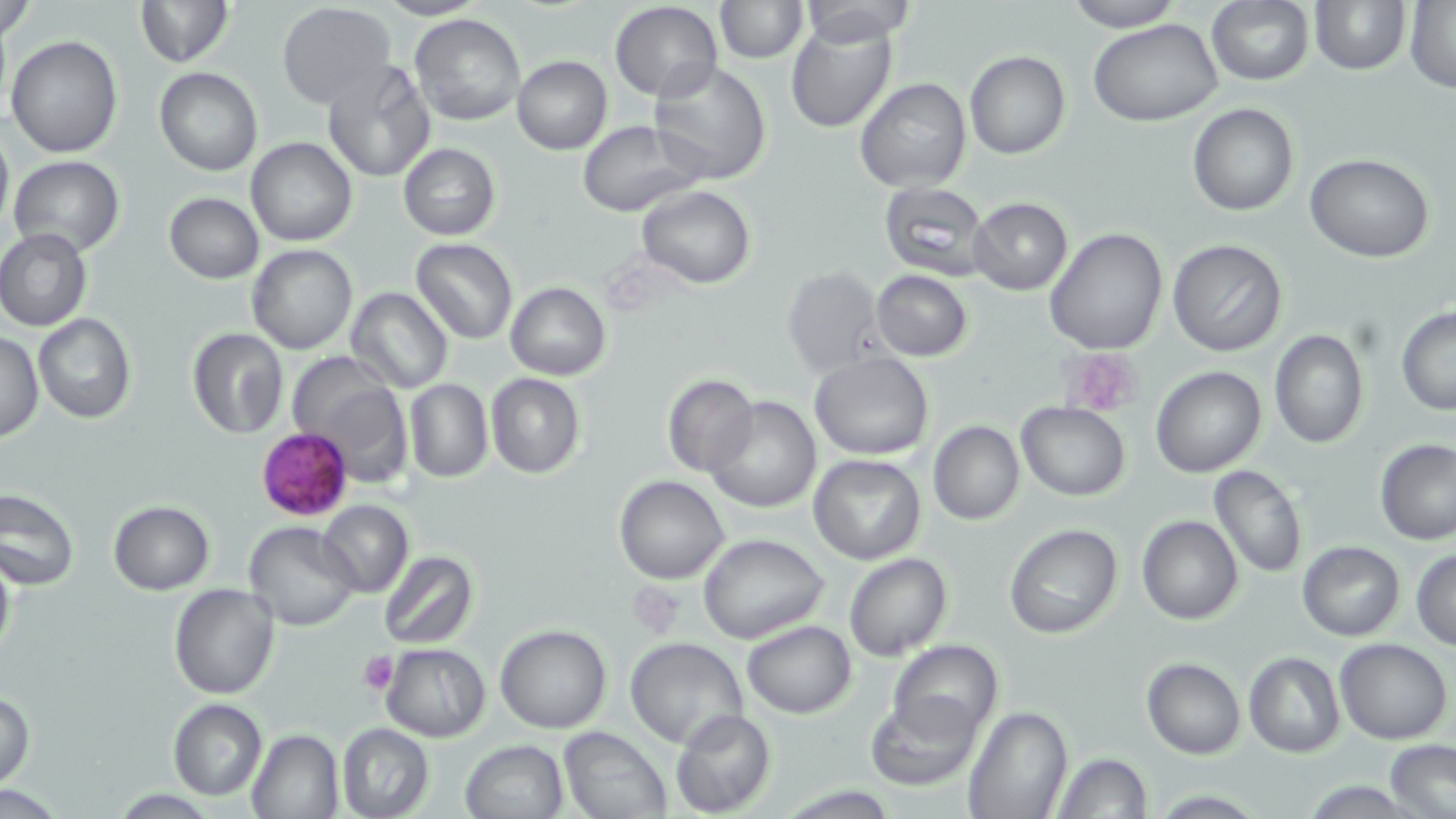

Summary:
  - Coordinate format: approximate bounding boxes as (x1, y1, x2, y2) in pixels
  - Plasmodium falciparum-infected red blood cell locations: (257, 427, 353, 518)
  - Uninfected red blood cell locations: (134, 0, 234, 67), (715, 0, 808, 63), (1309, 0, 1410, 74), (1, 1, 37, 44), (610, 1, 722, 100), (792, 1, 924, 45), (1064, 1, 1185, 31), (276, 2, 394, 110), (1206, 2, 1314, 85), (1403, 2, 1455, 92), (411, 14, 525, 126), (786, 16, 897, 133), (1089, 19, 1222, 126), (6, 33, 124, 157), (965, 50, 1071, 159), (512, 55, 612, 154), (645, 60, 770, 185), (321, 61, 435, 183), (155, 68, 263, 177), (854, 77, 971, 193), (1188, 103, 1298, 216), (576, 121, 701, 217), (0, 124, 13, 233), (245, 137, 357, 248), (398, 143, 500, 239), (1304, 153, 1435, 262), (8, 155, 127, 256), (878, 181, 992, 279), (637, 185, 756, 289), (164, 193, 264, 284), (970, 197, 1072, 293), (0, 227, 92, 332), (1044, 227, 1168, 355), (411, 238, 518, 345), (1168, 239, 1288, 356), (248, 244, 357, 354), (781, 265, 885, 379), (871, 270, 973, 361), (504, 282, 611, 380), (345, 286, 451, 393), (1395, 306, 1456, 414), (33, 314, 136, 423), (186, 328, 289, 440), (1268, 328, 1368, 448), (1, 329, 44, 442), (809, 351, 934, 459), (289, 358, 413, 486), (1151, 365, 1266, 478), (485, 372, 585, 479), (662, 373, 758, 476), (405, 379, 493, 483), (705, 395, 820, 512), (1015, 402, 1133, 500), (928, 422, 1025, 524), (1375, 439, 1455, 545), (808, 453, 926, 564), (1208, 465, 1307, 578), (614, 475, 729, 584), (0, 486, 78, 590), (317, 499, 413, 598), (108, 502, 213, 595), (1137, 515, 1244, 625), (244, 522, 361, 631), (1003, 522, 1125, 639), (698, 533, 829, 644), (1297, 541, 1405, 641), (0, 545, 15, 669), (1411, 548, 1456, 649), (377, 550, 477, 651), (843, 553, 952, 660), (170, 584, 278, 699), (742, 620, 857, 717), (495, 624, 612, 733), (625, 637, 747, 749), (888, 639, 1002, 739), (1335, 639, 1452, 744), (380, 643, 491, 742), (1243, 652, 1346, 757), (1141, 657, 1246, 758), (866, 692, 983, 790), (0, 693, 36, 788), (168, 698, 267, 801), (962, 704, 1071, 819), (670, 708, 776, 818), (337, 723, 434, 819), (558, 726, 672, 819), (245, 729, 344, 819), (460, 739, 568, 819), (1384, 740, 1455, 819), (1050, 752, 1153, 818)
  - Platelet locations: (1061, 350, 1144, 416), (358, 651, 397, 695)
  - Slide-level diagnosis: Plasmodium falciparum
  - Modality: light microscopy
  - Preparation: thin blood film
  - Stain: May-Grünwald-Giemsa
  - Field of view: one of a larger specimen
  - Image size: 1456×819 pixels
  - Magnification: 1000x